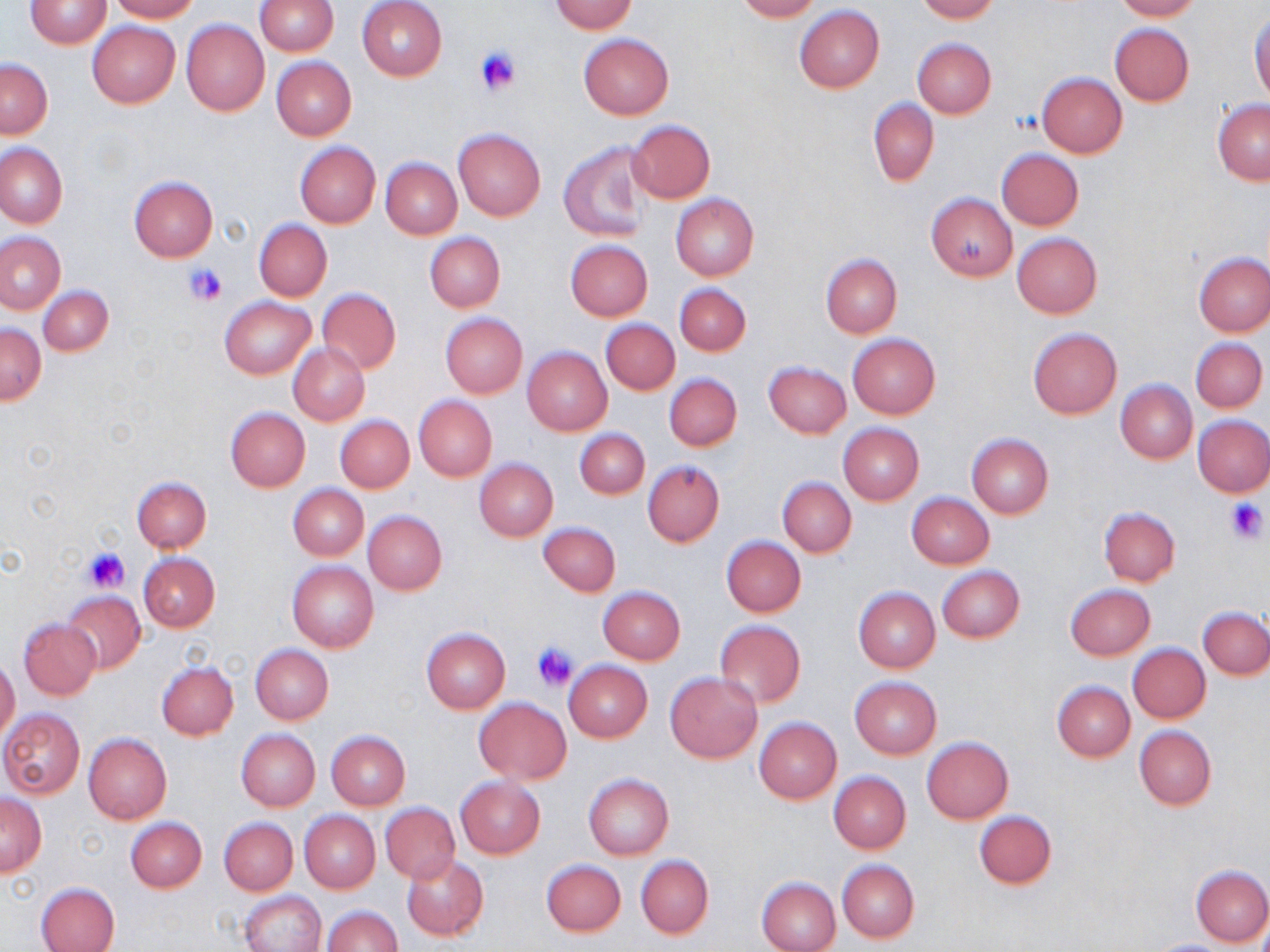

slide_level_diagnosis: no evidence of blood parasites
stain: May-Grünwald-Giemsa
magnification: 1000x
platelet_locations: 'approximate bounding boxes as named x1/y1/x2/y2 corners in pixels: (x1=476, y1=47, x2=523, y2=96), (x1=1012, y1=112, x2=1040, y2=134), (x1=185, y1=261, x2=228, y2=307), (x1=1225, y1=499, x2=1268, y2=542), (x1=82, y1=547, x2=128, y2=592), (x1=532, y1=640, x2=578, y2=691)'
preparation: thin blood smear
field_of_view: single
image_size: 1270×952 pixels
uninfected_red_blood_cell_locations: 'approximate bounding boxes as named x1/y1/x2/y2 corners in pixels: (x1=24, y1=0, x2=112, y2=48), (x1=107, y1=0, x2=201, y2=22), (x1=257, y1=0, x2=338, y2=55), (x1=356, y1=0, x2=447, y2=81), (x1=734, y1=0, x2=823, y2=22), (x1=915, y1=0, x2=998, y2=22), (x1=1113, y1=0, x2=1203, y2=21), (x1=548, y1=1, x2=637, y2=33), (x1=795, y1=6, x2=885, y2=92), (x1=1249, y1=9, x2=1270, y2=104), (x1=181, y1=19, x2=269, y2=116), (x1=86, y1=21, x2=181, y2=109), (x1=1109, y1=23, x2=1194, y2=105), (x1=578, y1=34, x2=674, y2=119), (x1=913, y1=38, x2=996, y2=117), (x1=272, y1=57, x2=356, y2=139), (x1=1, y1=59, x2=52, y2=138), (x1=1036, y1=73, x2=1127, y2=158), (x1=869, y1=99, x2=939, y2=186), (x1=1212, y1=99, x2=1270, y2=184), (x1=626, y1=119, x2=715, y2=204), (x1=453, y1=128, x2=546, y2=222), (x1=560, y1=141, x2=649, y2=242), (x1=295, y1=142, x2=380, y2=228), (x1=0, y1=143, x2=67, y2=227), (x1=995, y1=148, x2=1084, y2=230), (x1=380, y1=157, x2=462, y2=238), (x1=128, y1=176, x2=218, y2=261), (x1=671, y1=193, x2=759, y2=279), (x1=926, y1=193, x2=1016, y2=280), (x1=254, y1=218, x2=332, y2=301), (x1=0, y1=231, x2=64, y2=313), (x1=424, y1=232, x2=505, y2=312), (x1=1013, y1=232, x2=1102, y2=318), (x1=565, y1=240, x2=652, y2=320), (x1=1194, y1=251, x2=1270, y2=336), (x1=820, y1=253, x2=902, y2=338), (x1=674, y1=283, x2=750, y2=355), (x1=38, y1=285, x2=113, y2=357), (x1=317, y1=290, x2=399, y2=374), (x1=219, y1=296, x2=316, y2=379), (x1=440, y1=313, x2=528, y2=398), (x1=600, y1=318, x2=679, y2=395), (x1=0, y1=324, x2=45, y2=404), (x1=1027, y1=328, x2=1121, y2=418), (x1=847, y1=333, x2=940, y2=419), (x1=1190, y1=338, x2=1267, y2=413), (x1=289, y1=343, x2=370, y2=425), (x1=522, y1=347, x2=612, y2=435), (x1=764, y1=362, x2=851, y2=438), (x1=664, y1=373, x2=742, y2=451), (x1=1115, y1=380, x2=1197, y2=463), (x1=414, y1=396, x2=496, y2=481), (x1=225, y1=407, x2=310, y2=491), (x1=336, y1=415, x2=415, y2=493), (x1=1194, y1=415, x2=1270, y2=497), (x1=838, y1=423, x2=923, y2=505), (x1=574, y1=428, x2=649, y2=501), (x1=966, y1=433, x2=1053, y2=519), (x1=475, y1=459, x2=557, y2=541), (x1=643, y1=460, x2=725, y2=547), (x1=131, y1=476, x2=211, y2=552), (x1=777, y1=476, x2=857, y2=557), (x1=288, y1=484, x2=369, y2=562), (x1=907, y1=492, x2=994, y2=568), (x1=1099, y1=506, x2=1180, y2=587), (x1=363, y1=510, x2=446, y2=595), (x1=538, y1=521, x2=621, y2=597), (x1=721, y1=536, x2=806, y2=618), (x1=137, y1=552, x2=220, y2=632), (x1=287, y1=561, x2=378, y2=653), (x1=937, y1=566, x2=1025, y2=644), (x1=1066, y1=584, x2=1155, y2=660), (x1=597, y1=586, x2=685, y2=664), (x1=853, y1=586, x2=940, y2=672), (x1=62, y1=591, x2=146, y2=674), (x1=1199, y1=607, x2=1270, y2=679), (x1=19, y1=620, x2=101, y2=701), (x1=714, y1=620, x2=807, y2=708), (x1=421, y1=628, x2=510, y2=712), (x1=250, y1=644, x2=333, y2=724), (x1=1128, y1=644, x2=1210, y2=723), (x1=0, y1=657, x2=20, y2=743), (x1=563, y1=660, x2=652, y2=743), (x1=156, y1=661, x2=238, y2=740), (x1=665, y1=672, x2=762, y2=763), (x1=849, y1=677, x2=941, y2=758), (x1=1051, y1=681, x2=1135, y2=761), (x1=474, y1=698, x2=571, y2=784), (x1=0, y1=708, x2=85, y2=800), (x1=755, y1=718, x2=841, y2=803), (x1=1135, y1=725, x2=1216, y2=810), (x1=236, y1=729, x2=320, y2=810), (x1=326, y1=730, x2=410, y2=809), (x1=83, y1=733, x2=171, y2=823), (x1=922, y1=737, x2=1013, y2=822), (x1=829, y1=771, x2=911, y2=853), (x1=583, y1=774, x2=673, y2=859), (x1=456, y1=777, x2=545, y2=858), (x1=0, y1=793, x2=48, y2=876), (x1=380, y1=802, x2=459, y2=884), (x1=298, y1=810, x2=380, y2=893), (x1=973, y1=810, x2=1057, y2=889), (x1=125, y1=817, x2=207, y2=893), (x1=219, y1=818, x2=297, y2=895), (x1=636, y1=854, x2=714, y2=938), (x1=401, y1=855, x2=488, y2=940), (x1=541, y1=859, x2=626, y2=936), (x1=837, y1=859, x2=919, y2=943), (x1=1190, y1=865, x2=1270, y2=947), (x1=756, y1=876, x2=840, y2=952), (x1=34, y1=881, x2=119, y2=952), (x1=239, y1=890, x2=325, y2=952), (x1=321, y1=905, x2=401, y2=952)'
modality: optical microscopy